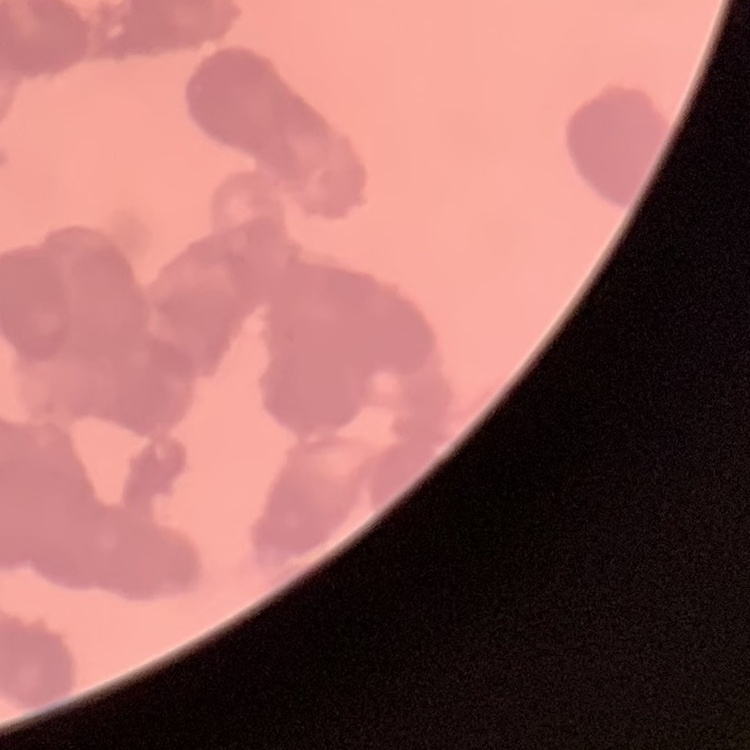
The erythrocytes exhibit rouleaux formation. Stained with either Field's or Giemsa. One tile cut from a larger photomicrograph. Thin blood film.